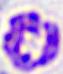
Micrograph. A white blood cell is shown. Captured at 400x magnification.